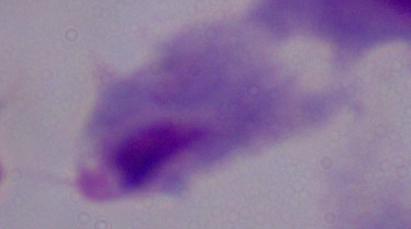 Micrograph. A trichomonad is seen. Captured at 1000x magnification.